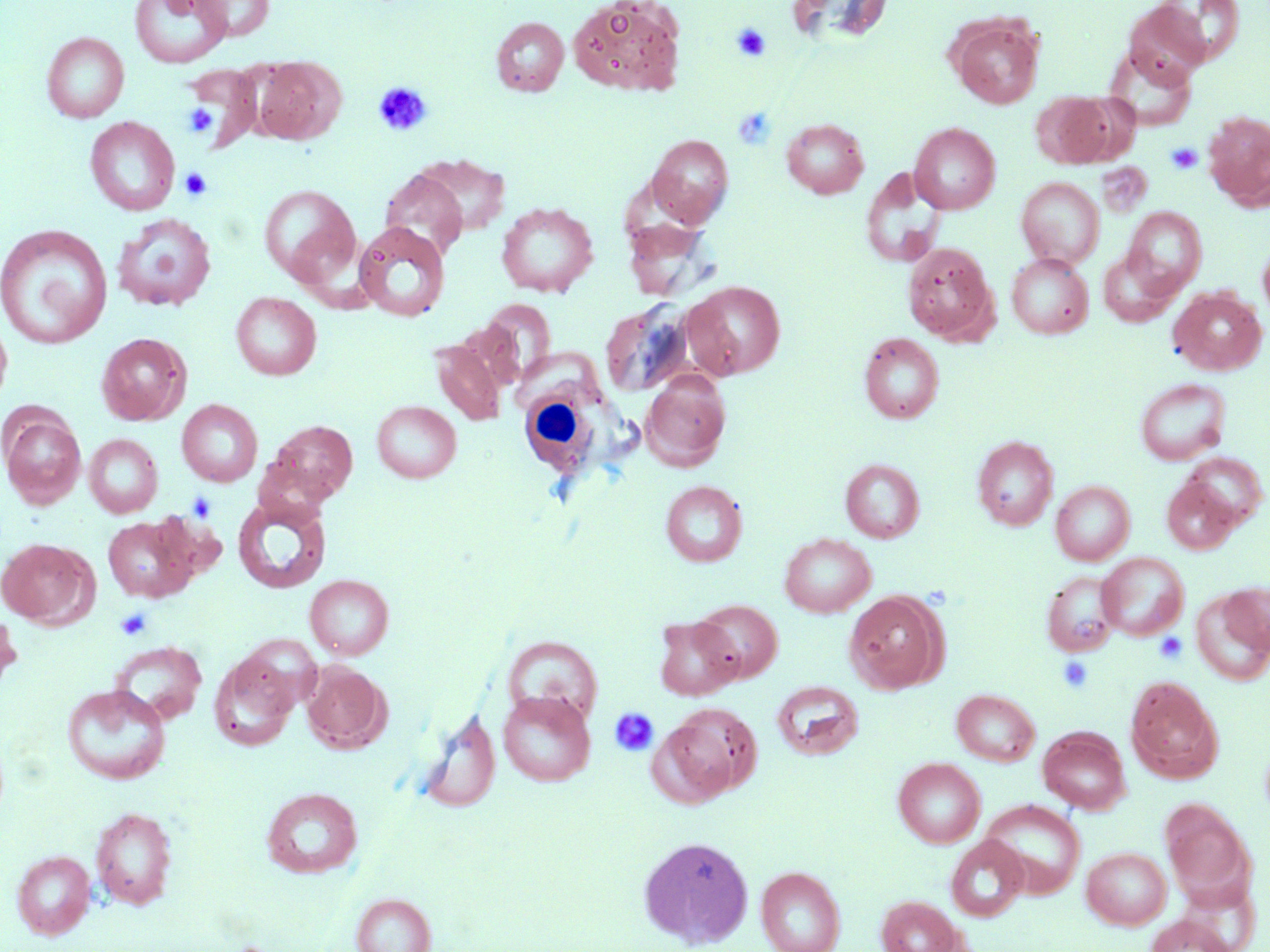

slide-level diagnosis = negative for blood parasites
platelet locations = approximate bounding boxes as (x1, y1, x2, y2) in pixels: (732, 24, 771, 62), (374, 82, 433, 136), (183, 103, 217, 139), (732, 106, 777, 150), (1166, 142, 1203, 174), (179, 168, 211, 201), (188, 491, 216, 522), (115, 608, 152, 640), (1153, 631, 1189, 665), (1057, 656, 1095, 694), (609, 707, 659, 757)
image size = 1270×952 pixels
modality = optical microscopy
preparation = thin blood film
stain = May-Grünwald-Giemsa
white blood cell locations = approximate bounding boxes as (x1, y1, x2, y2) in pixels: (518, 388, 613, 478)
uninfected red blood cell locations = approximate bounding boxes as (x1, y1, x2, y2) in pixels: (129, 0, 231, 68), (191, 0, 274, 41), (568, 0, 686, 95), (786, 1, 892, 48), (1124, 6, 1212, 86), (490, 17, 569, 96), (949, 17, 1044, 109), (41, 32, 129, 123), (1105, 47, 1198, 130), (251, 55, 344, 145), (185, 63, 262, 149), (1033, 91, 1127, 168), (1203, 111, 1270, 207), (84, 116, 180, 216), (781, 118, 869, 199), (910, 123, 1000, 214), (647, 134, 733, 227), (412, 154, 511, 237), (380, 169, 468, 259), (860, 169, 945, 269), (1016, 178, 1104, 268), (259, 184, 360, 286), (496, 201, 598, 297), (1122, 206, 1207, 297), (112, 213, 216, 312), (1, 223, 113, 350), (354, 223, 450, 322), (1258, 240, 1270, 326), (903, 242, 997, 343), (1099, 249, 1180, 326), (1007, 253, 1093, 339), (683, 281, 786, 379), (1168, 287, 1266, 375), (231, 292, 321, 381), (477, 299, 557, 384), (601, 301, 694, 398), (0, 308, 13, 411), (859, 332, 944, 424), (96, 333, 191, 425), (430, 336, 508, 427), (640, 370, 731, 470), (1135, 378, 1231, 465), (177, 399, 263, 486), (372, 401, 461, 483), (1, 410, 86, 509), (268, 420, 358, 503), (84, 434, 162, 517), (973, 435, 1058, 530), (1183, 453, 1267, 530), (840, 458, 925, 543), (1162, 477, 1240, 554), (660, 480, 747, 566), (1051, 480, 1135, 565), (232, 497, 331, 594), (102, 515, 198, 602), (780, 533, 876, 617), (0, 537, 96, 627), (1097, 552, 1189, 640), (1041, 570, 1122, 657), (305, 574, 394, 660), (1220, 582, 1270, 653), (844, 590, 945, 694), (1192, 590, 1269, 685), (692, 599, 782, 683), (0, 609, 22, 695), (653, 616, 741, 700), (503, 636, 602, 727), (110, 641, 207, 724), (209, 651, 298, 752), (301, 661, 390, 753), (1126, 677, 1222, 783), (771, 681, 864, 760), (61, 684, 171, 785), (951, 689, 1039, 766), (498, 691, 595, 786), (657, 706, 758, 802), (415, 707, 501, 813), (1038, 727, 1131, 814), (893, 757, 985, 848), (261, 787, 363, 877), (980, 801, 1085, 898), (1161, 801, 1251, 900), (90, 806, 178, 910), (638, 835, 753, 949), (946, 836, 1029, 922), (1082, 847, 1171, 929), (11, 850, 96, 938), (756, 865, 846, 952), (1176, 882, 1261, 950), (351, 893, 436, 952), (877, 895, 962, 952), (1144, 915, 1237, 952)
magnification = 1000x
field of view = one of a larger specimen